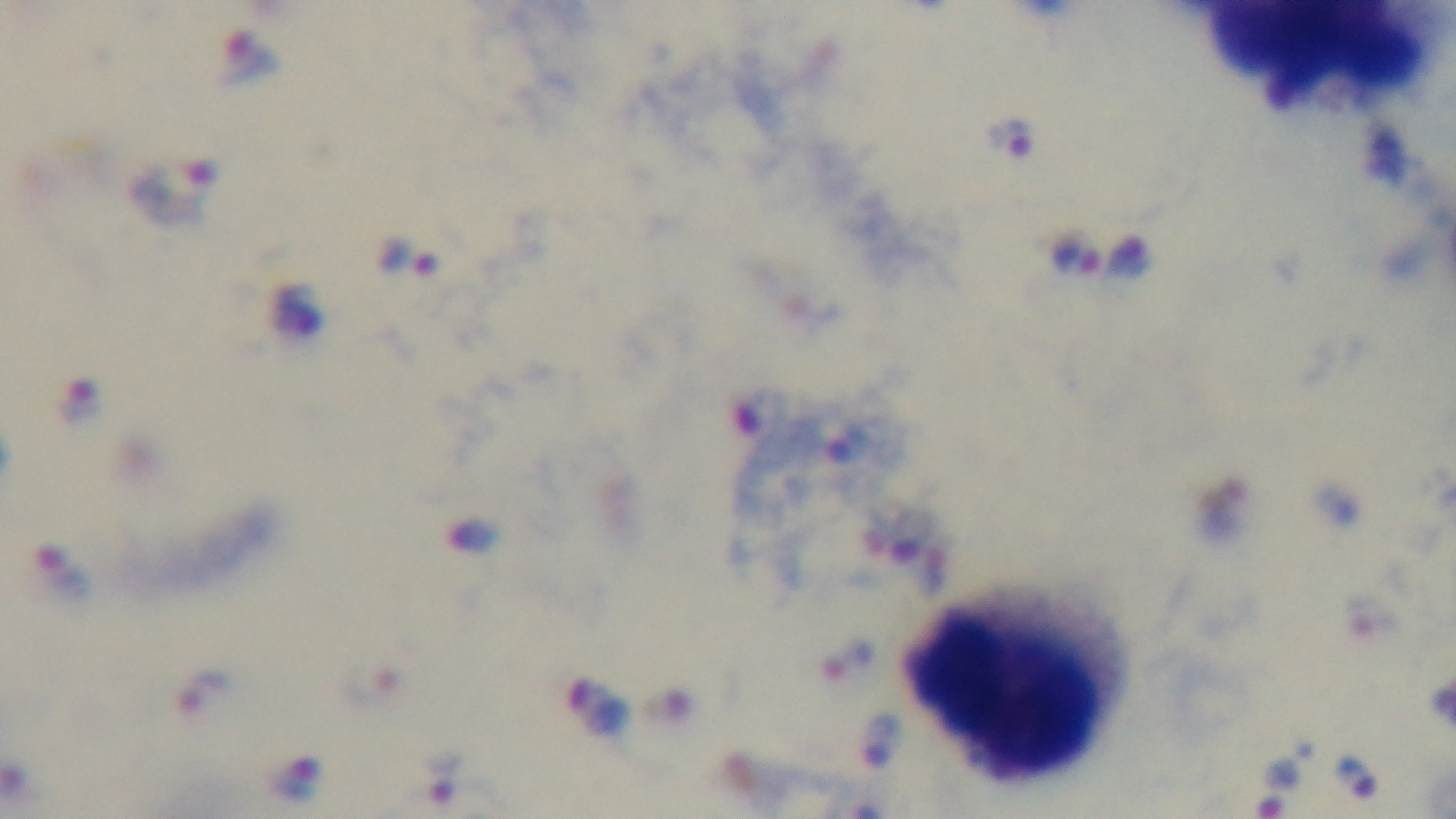

Summary:
  - Objective: 100x oil immersion
  - Stain: Giemsa
  - Modality: light microscopy
  - Capture: mounted 4K digital camera
  - Preparation: thick blood film
  - Malaria status: positive
  - Field of view: one from the slide